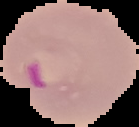

From a thin blood film. Image is 139×127 pixels. Malaria status: parasitized. Segmented cell region on a black background.